Identify the blood parasite species.
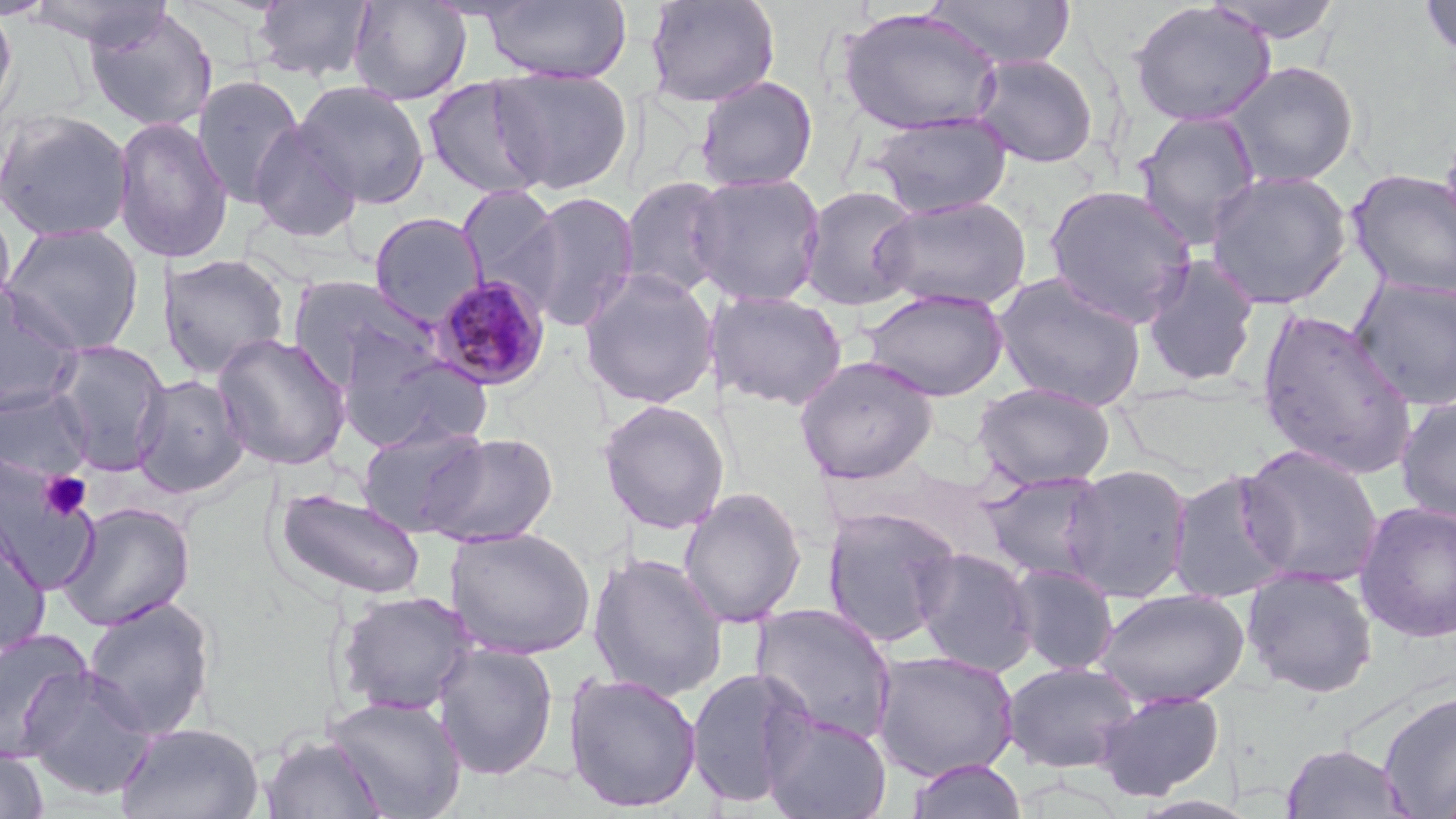
Plasmodium malariae.

Summary:
  - Coordinate format: approximate bounding boxes as named x1/y1/x2/y2 corners in pixels
  - Uninfected red blood cell locations: (x1=0, y1=0, x2=19, y2=132), (x1=25, y1=0, x2=173, y2=49), (x1=251, y1=0, x2=376, y2=84), (x1=347, y1=0, x2=472, y2=105), (x1=480, y1=0, x2=632, y2=84), (x1=644, y1=0, x2=780, y2=108), (x1=926, y1=0, x2=1076, y2=70), (x1=1206, y1=0, x2=1345, y2=43), (x1=1420, y1=0, x2=1455, y2=61), (x1=1128, y1=2, x2=1276, y2=128), (x1=84, y1=6, x2=219, y2=133), (x1=838, y1=8, x2=1004, y2=137), (x1=970, y1=54, x2=1099, y2=168), (x1=1223, y1=61, x2=1359, y2=188), (x1=488, y1=67, x2=632, y2=195), (x1=191, y1=74, x2=306, y2=208), (x1=695, y1=75, x2=818, y2=192), (x1=423, y1=77, x2=549, y2=200), (x1=293, y1=80, x2=431, y2=210), (x1=0, y1=109, x2=135, y2=243), (x1=1134, y1=110, x2=1262, y2=247), (x1=868, y1=111, x2=1013, y2=219), (x1=112, y1=116, x2=233, y2=263), (x1=248, y1=122, x2=363, y2=243), (x1=1346, y1=168, x2=1456, y2=299), (x1=1204, y1=170, x2=1353, y2=310), (x1=688, y1=171, x2=827, y2=307), (x1=619, y1=176, x2=733, y2=299), (x1=1044, y1=183, x2=1198, y2=328), (x1=457, y1=184, x2=566, y2=305), (x1=799, y1=185, x2=922, y2=311), (x1=517, y1=192, x2=639, y2=332), (x1=873, y1=195, x2=1031, y2=312), (x1=0, y1=198, x2=17, y2=321), (x1=369, y1=212, x2=486, y2=326), (x1=1, y1=223, x2=145, y2=356), (x1=157, y1=253, x2=291, y2=380), (x1=1140, y1=254, x2=1261, y2=389), (x1=579, y1=269, x2=719, y2=409), (x1=993, y1=272, x2=1147, y2=411), (x1=288, y1=275, x2=440, y2=395), (x1=1348, y1=276, x2=1456, y2=411), (x1=0, y1=284, x2=83, y2=417), (x1=862, y1=287, x2=1009, y2=401), (x1=710, y1=290, x2=848, y2=410), (x1=1256, y1=308, x2=1418, y2=479), (x1=212, y1=332, x2=352, y2=471), (x1=48, y1=339, x2=171, y2=475), (x1=346, y1=350, x2=494, y2=452), (x1=794, y1=355, x2=938, y2=485), (x1=132, y1=373, x2=249, y2=499), (x1=971, y1=382, x2=1116, y2=490), (x1=0, y1=386, x2=94, y2=482), (x1=1395, y1=396, x2=1456, y2=524), (x1=596, y1=398, x2=730, y2=535), (x1=356, y1=422, x2=490, y2=536), (x1=419, y1=431, x2=558, y2=547), (x1=1239, y1=444, x2=1384, y2=589), (x1=0, y1=458, x2=97, y2=590), (x1=1060, y1=464, x2=1194, y2=602), (x1=1166, y1=468, x2=1296, y2=603), (x1=980, y1=471, x2=1113, y2=583), (x1=677, y1=487, x2=807, y2=628), (x1=274, y1=488, x2=426, y2=601), (x1=57, y1=501, x2=196, y2=632), (x1=1354, y1=501, x2=1456, y2=643), (x1=821, y1=506, x2=961, y2=648), (x1=0, y1=514, x2=51, y2=660), (x1=445, y1=526, x2=596, y2=660), (x1=912, y1=547, x2=1038, y2=677), (x1=587, y1=552, x2=729, y2=700), (x1=1007, y1=563, x2=1120, y2=675), (x1=1241, y1=566, x2=1379, y2=698), (x1=1095, y1=588, x2=1249, y2=708), (x1=334, y1=590, x2=479, y2=717), (x1=81, y1=596, x2=217, y2=740), (x1=750, y1=603, x2=899, y2=747), (x1=0, y1=629, x2=96, y2=762), (x1=432, y1=643, x2=559, y2=781), (x1=871, y1=650, x2=1020, y2=781), (x1=1001, y1=660, x2=1140, y2=773), (x1=20, y1=666, x2=157, y2=801), (x1=685, y1=666, x2=816, y2=809), (x1=563, y1=672, x2=702, y2=813), (x1=1095, y1=689, x2=1226, y2=801), (x1=1377, y1=691, x2=1456, y2=818), (x1=325, y1=694, x2=468, y2=816), (x1=761, y1=710, x2=892, y2=819), (x1=115, y1=721, x2=265, y2=819), (x1=259, y1=733, x2=388, y2=818), (x1=1279, y1=742, x2=1414, y2=818), (x1=1, y1=745, x2=49, y2=818), (x1=907, y1=757, x2=1028, y2=819), (x1=1435, y1=763, x2=1456, y2=819), (x1=1130, y1=795, x2=1259, y2=819)
  - Plasmodium malariae-infected red blood cell locations: (x1=429, y1=274, x2=552, y2=391)
  - Platelet locations: (x1=39, y1=471, x2=91, y2=520)
  - Stain: May-Grünwald-Giemsa
  - Field of view: single
  - Preparation: thin blood film
  - Magnification: 1000x
  - Image size: 1456×819 pixels
  - Modality: light microscopy